Describe the morphology of the red blood cells.
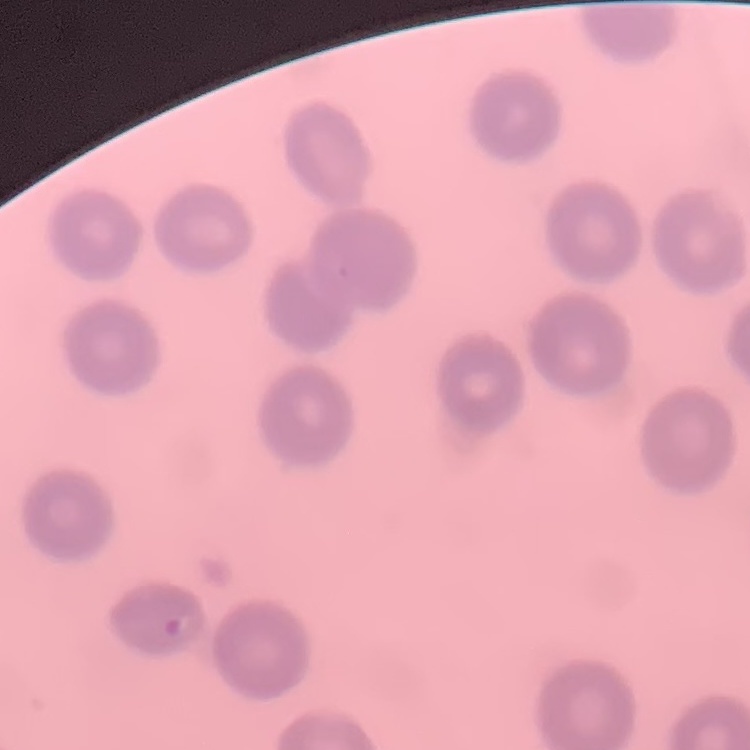
No rouleaux formation.

Stained with either Field's or Giemsa. One tile cut from a larger photomicrograph. Thin blood smear.